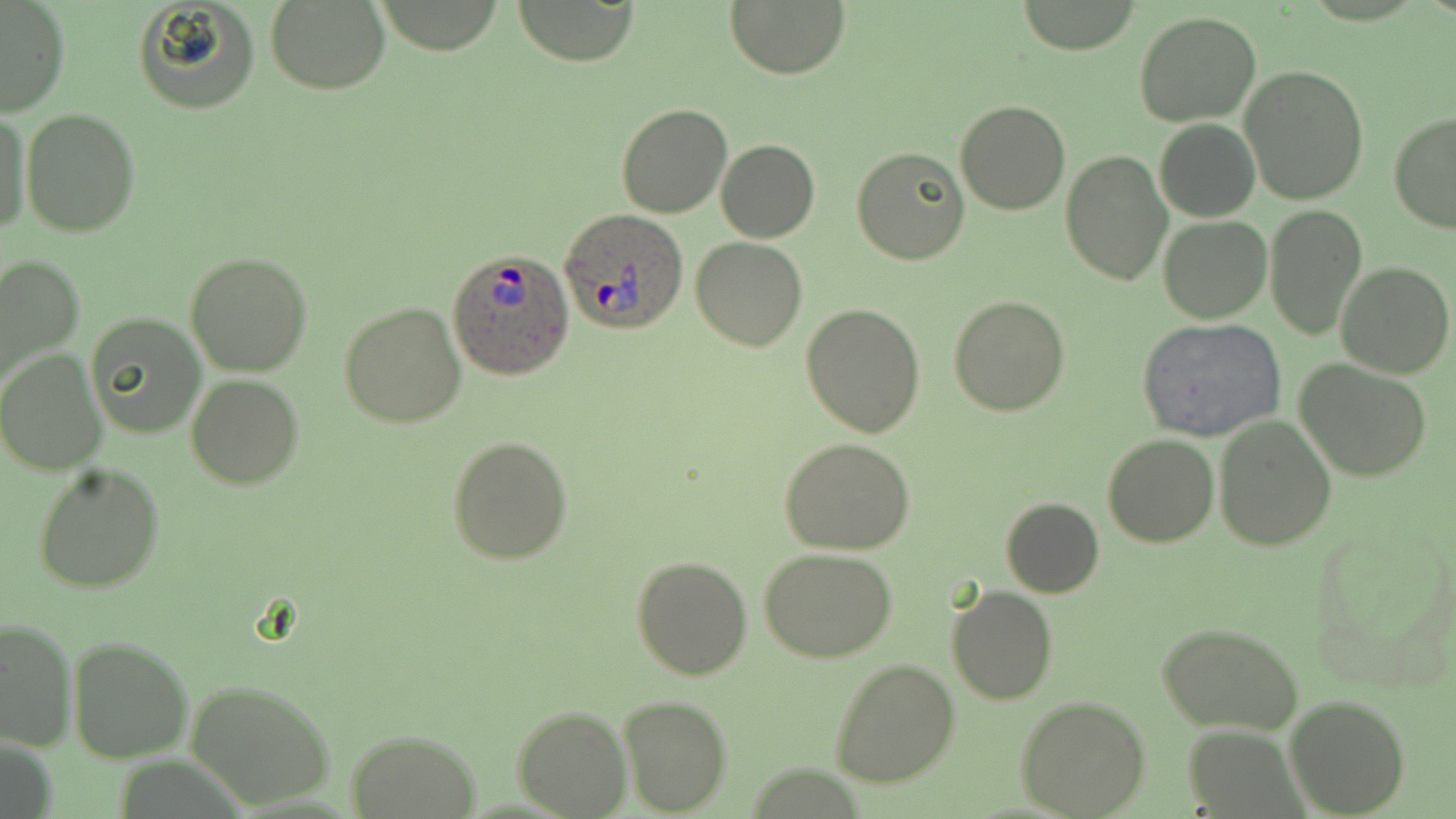
Summary:
  - Coordinate format: approximate bounding boxes as (x1,y1)-(x2,y2) corner pairs in pixels
  - Plasmodium ovale-infected red blood cell locations: (559,209)-(689,335), (447,250)-(576,379)
  - Uninfected red blood cell locations: (134,0)-(262,115), (1017,0)-(1144,54), (510,1)-(641,65), (726,1)-(850,79), (0,2)-(70,118), (264,2)-(389,94), (1134,11)-(1261,126), (1240,64)-(1370,206), (955,101)-(1071,217), (616,103)-(734,219), (21,107)-(140,236), (0,110)-(31,238), (1387,111)-(1456,234), (1153,118)-(1260,222), (717,138)-(820,243), (852,145)-(969,264), (1060,150)-(1172,286), (1264,205)-(1367,340), (1158,215)-(1271,323), (691,237)-(809,352), (185,250)-(312,376), (0,253)-(85,393), (1335,262)-(1454,378), (949,295)-(1070,416), (339,302)-(466,428), (801,302)-(925,438), (87,311)-(206,439), (1137,318)-(1286,442), (0,348)-(106,476), (1293,359)-(1433,482), (186,374)-(304,490), (1214,416)-(1335,551), (1103,433)-(1218,548), (446,435)-(573,566), (780,437)-(916,553), (33,462)-(164,593), (1000,498)-(1103,598), (759,547)-(900,662), (631,554)-(753,680), (946,586)-(1058,706), (1,615)-(76,752), (1157,620)-(1304,736), (68,637)-(192,764), (830,657)-(961,789), (185,679)-(339,810), (617,695)-(732,816), (1284,695)-(1411,817), (1014,696)-(1151,818), (514,706)-(631,818), (346,728)-(481,819)
  - Slide-level diagnosis: Plasmodium ovale
  - Stain: May-Grünwald-Giemsa
  - Magnification: 1000x
  - Image size: 1456×819 pixels
  - Preparation: thin blood smear
  - Modality: light microscopy
  - Field of view: one of a larger specimen